Identify the parasite.
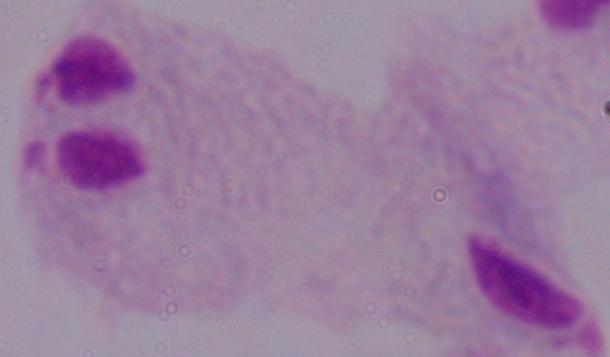
A trichomonad.

Summary:
  - Magnification: 1000x
  - Modality: micrograph